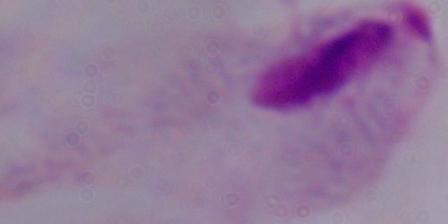

{
  "magnification": "1000x",
  "modality": "photomicrograph",
  "identification": "trichomonad"
}